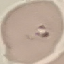 Malaria status: parasitized. Cell patch, automatically extracted from a larger field of view and resized to 64 × 64 pixels. Photographed with a smartphone camera at the microscope eyepiece. Thin smear of blood. Giemsa stain.